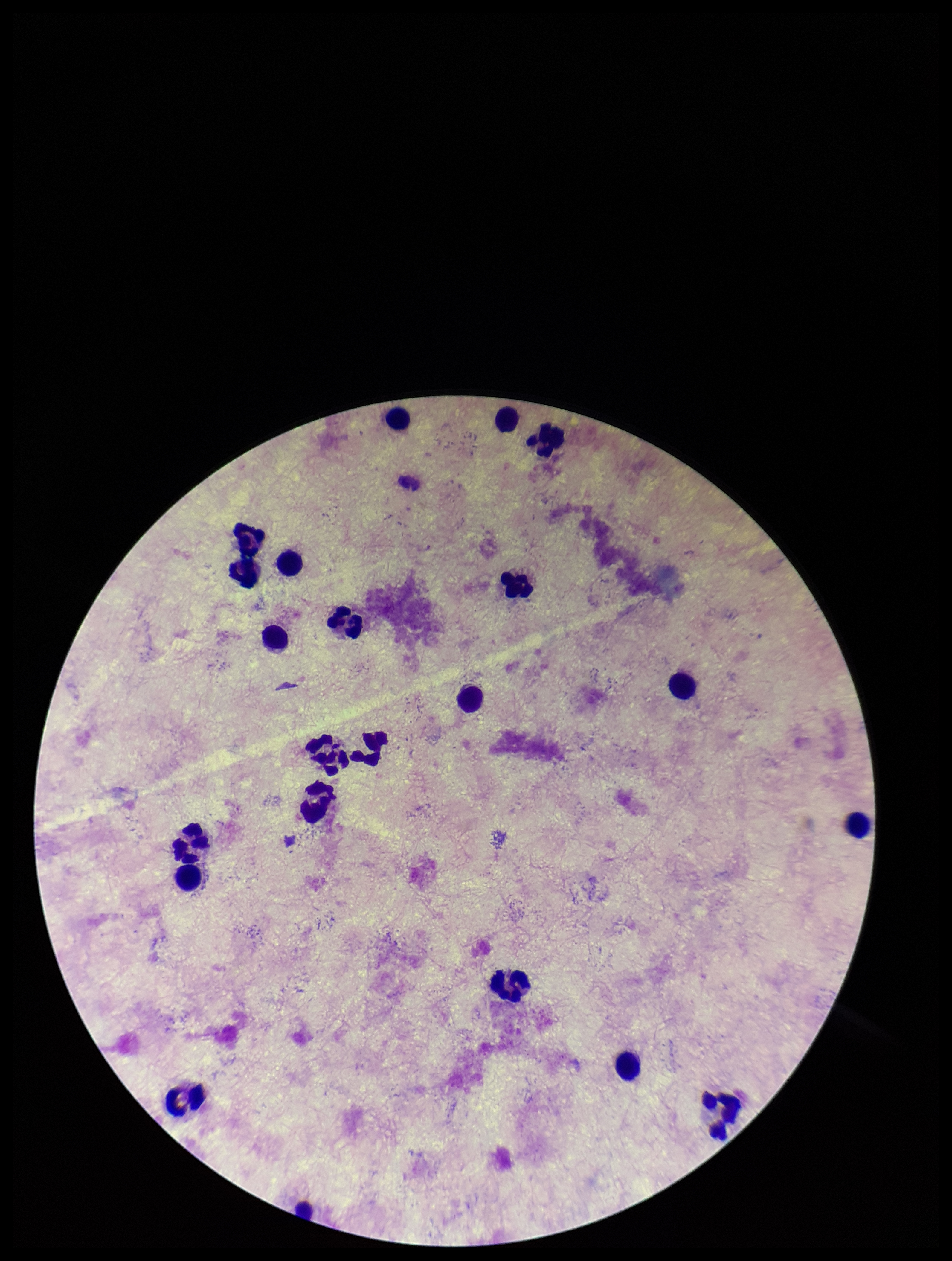

parasite count = 0
Plasmodium parasites = none detected
leukocyte count = 22
image size = 952×1261 pixels
preparation = thick smear
patient malaria status = negative
capture = smartphone photograph through the microscope eyepiece
stain = Giemsa
field of view = single